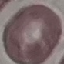

Summary:
  - Malaria status: uninfected
  - Stain: Giemsa
  - Preparation: thin smear
  - Capture: smartphone camera at the microscope eyepiece
  - Image type: automatically extracted cell patch, resized to 64 × 64 pixels